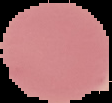
Summary:
  - Image type: segmented cell region on a black background
  - Result: no Plasmodium parasites seen
  - Preparation: thin blood film
  - Image size: 112×103 pixels